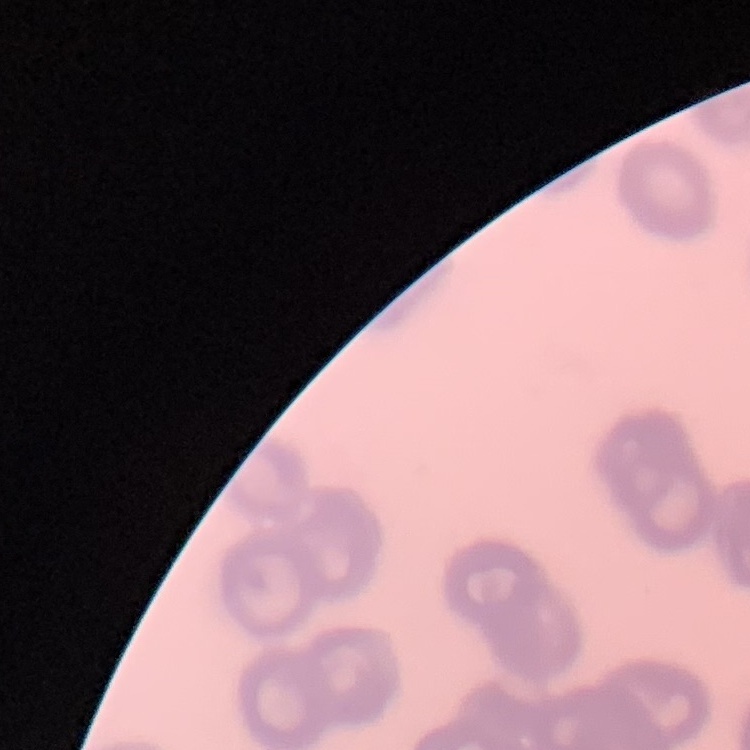

Summary:
  - Red blood cell morphology: rouleaux formation
  - Preparation: thin blood film
  - Image type: one tile cut from a larger photomicrograph
  - Stain: Field's or Giemsa